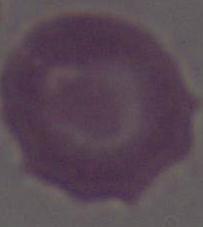
identification = erythrocyte
modality = photomicrograph
magnification = 1000x